Give the preparation type.
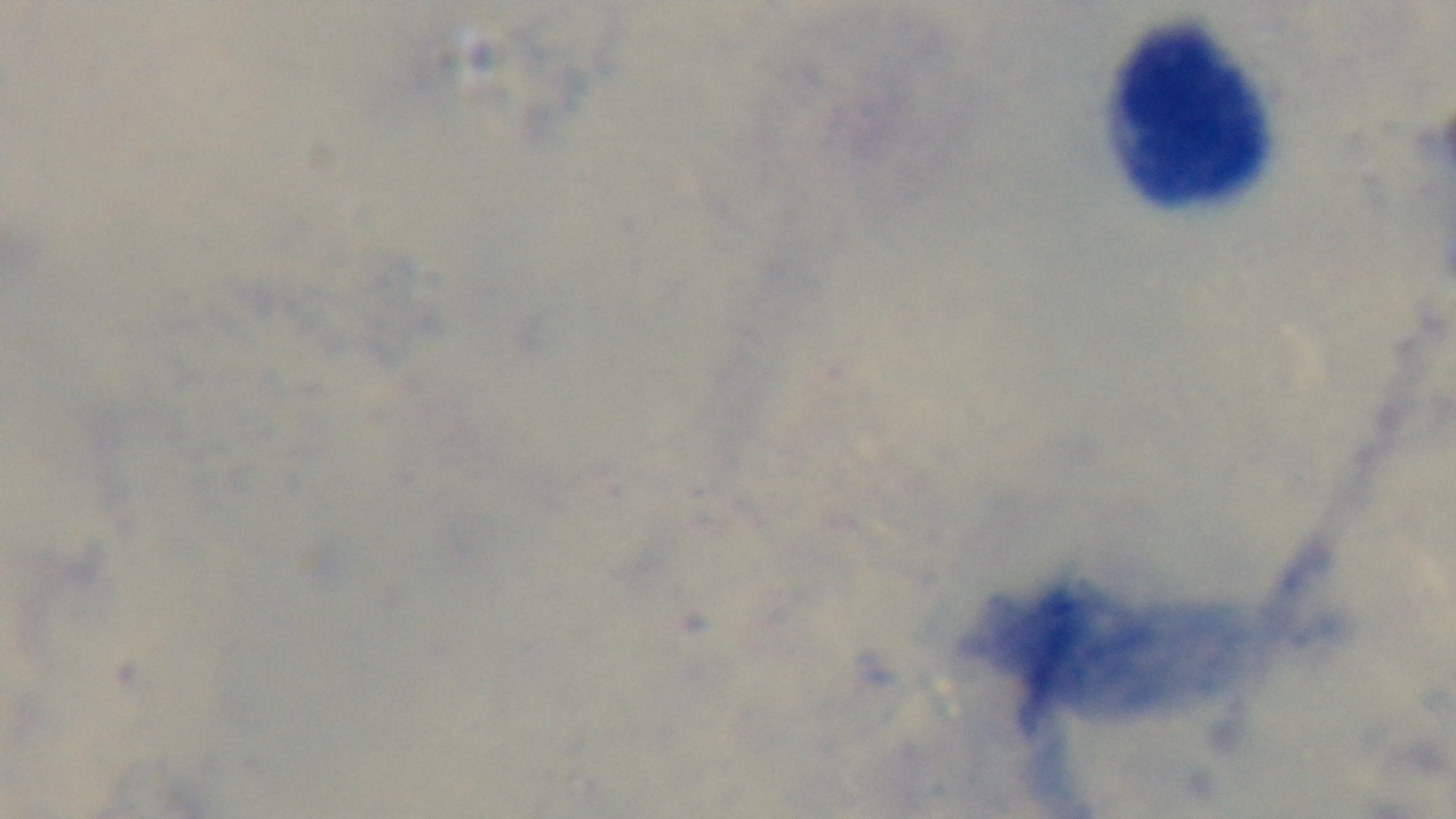
It is a thick blood film.

Oil-immersion objective, 100x. Photomicrograph. One field from the slide. Giemsa stain. Malaria status: negative. Captured with a mounted 4K digital camera.